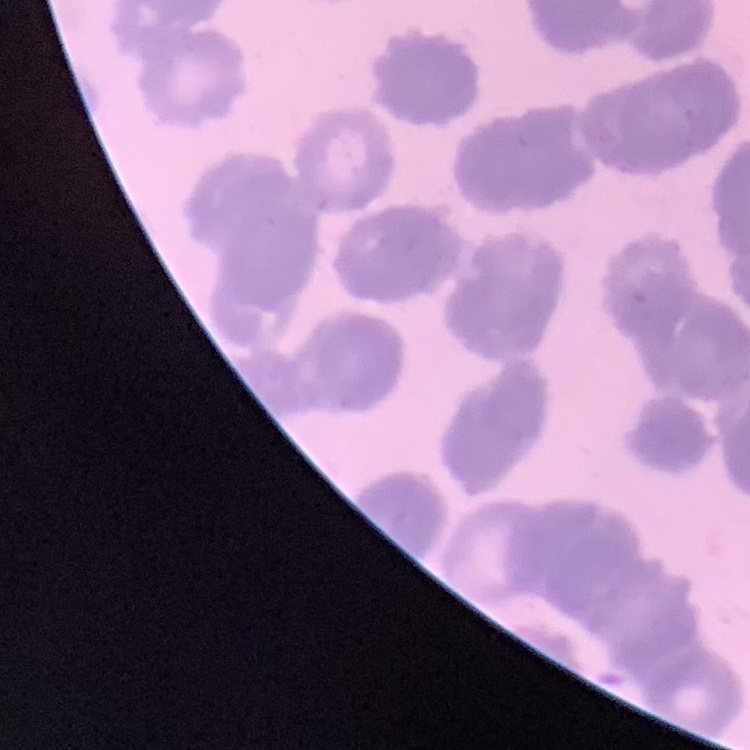
red_blood_cell_morphology: rouleaux formation
image_type: square crop of a larger photomicrograph
preparation: thin peripheral smear
stain: Field's or Giemsa